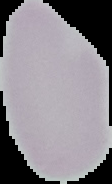
Malaria status: uninfected. The area outside the segmented cell region is set to black. From a thin blood smear. Image is 112×184 pixels.